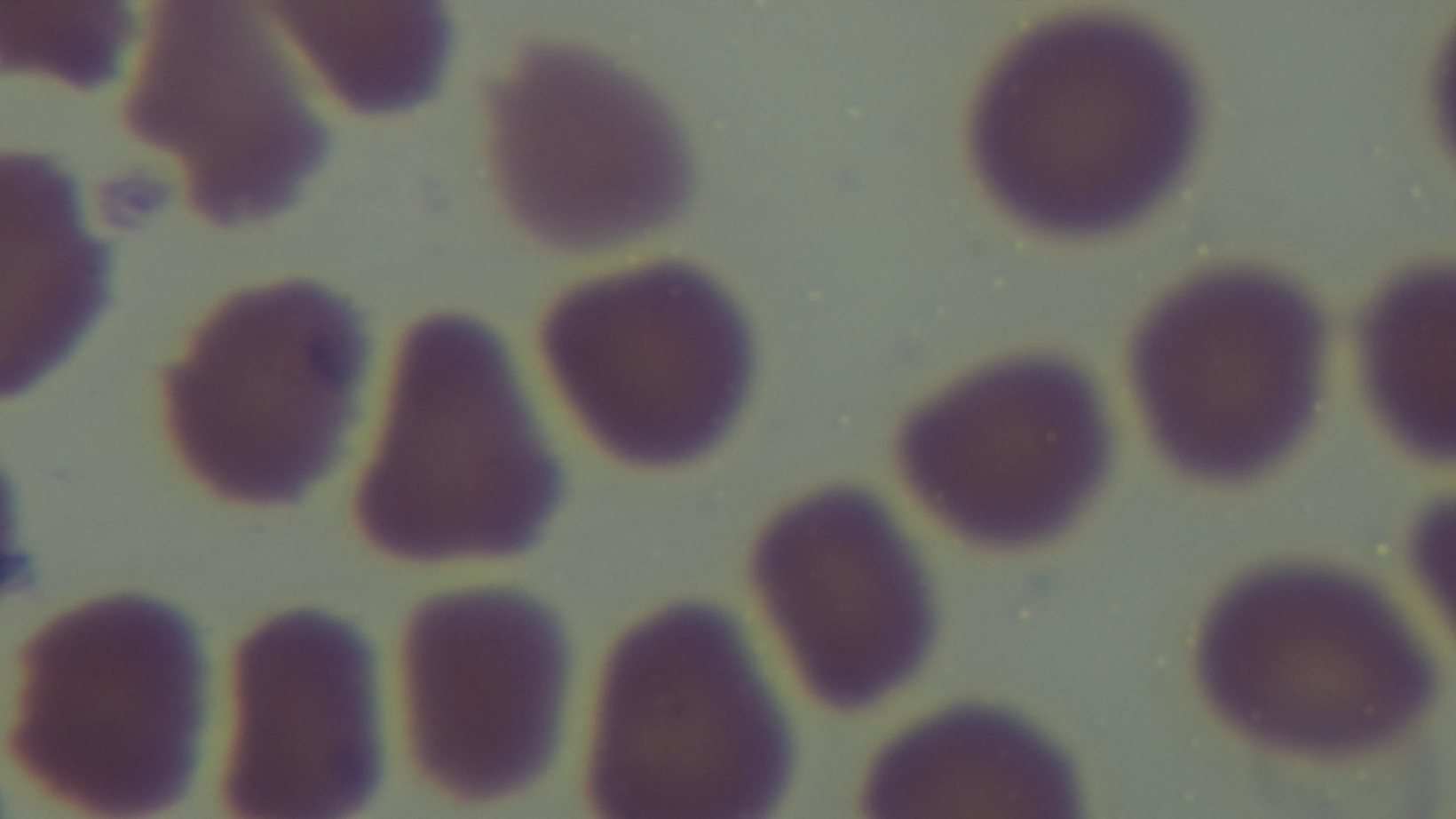

field of view = one from the slide
modality = light microscopy
objective = 100x oil immersion
stain = Giemsa
capture = mounted 4K digital camera
preparation = thin
malaria status = negative